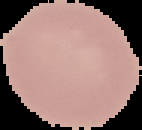 Image is 142×130 pixels. Malaria status: uninfected. Segmented cell region on a black background. From a thin blood smear.